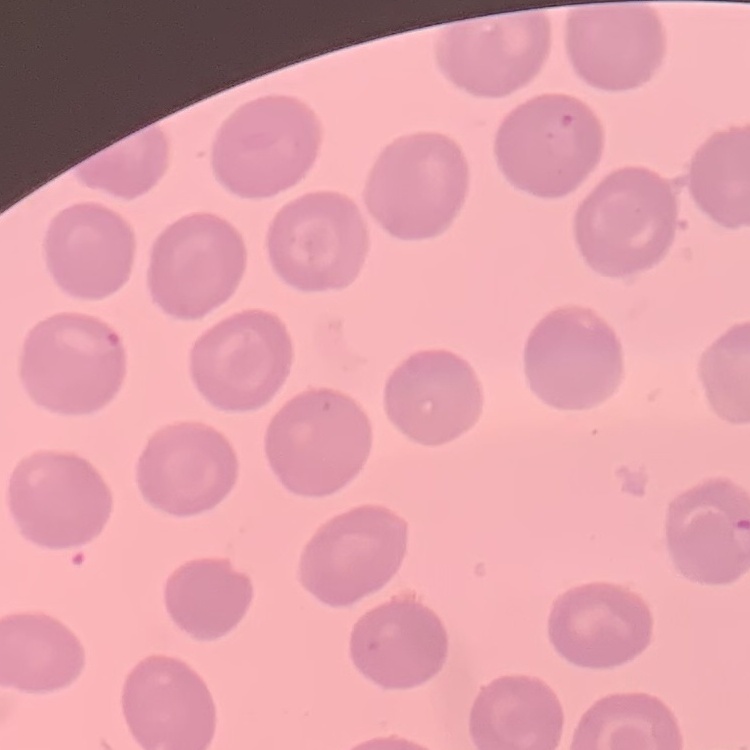
The erythrocytes exhibit no rouleaux formation. Thin blood smear. One tile cut from a larger photomicrograph. Stained with either Field's or Giemsa.